Report the malaria status of this cell.
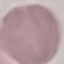

It is uninfected.

Thin blood smear. Giemsa stain. Cell patch, automatically extracted from a larger field of view and resized to 64 × 64 pixels. Acquired by smartphone through the microscope eyepiece.